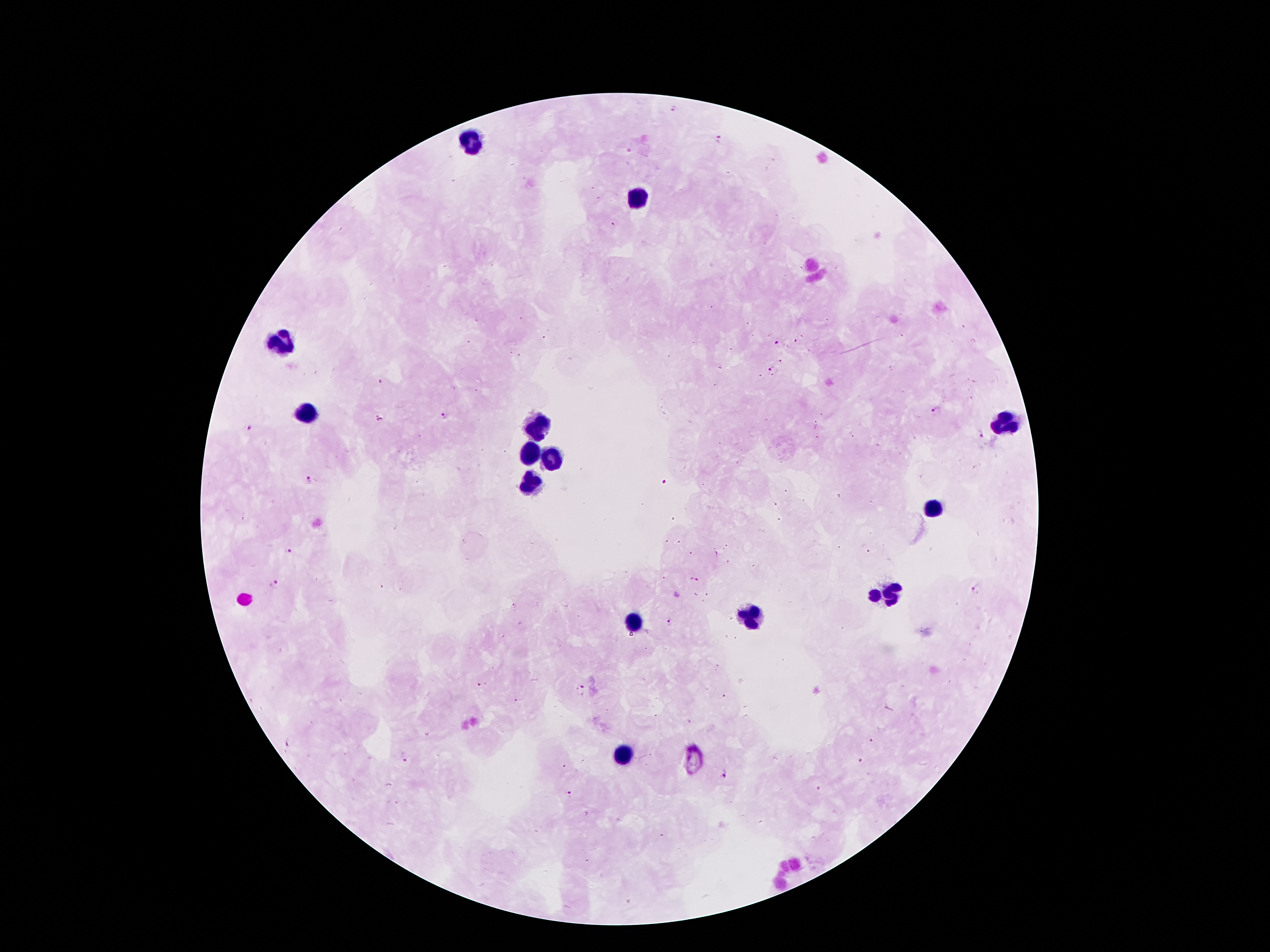

Approximate centers as [x, y] in pixels. Plasmodium parasite locations: [673, 109], [719, 139], [614, 224], [781, 342], [781, 359], [720, 367], [772, 370], [381, 382], [938, 411], [445, 416], [378, 417], [250, 427], [980, 435], [309, 481], [664, 482], [292, 551], [715, 554], [692, 578], [698, 580], [276, 584], [978, 587], [677, 595], [515, 607], [670, 622], [647, 632], [478, 684], [582, 686], [519, 700], [872, 740], [289, 742], [406, 758], [862, 761], [565, 767], [725, 776], [817, 789], [572, 793]. Leukocyte locations: [470, 136], [638, 201], [279, 346], [310, 413], [1007, 422], [537, 425], [531, 450], [554, 458], [528, 481], [932, 509], [876, 593], [893, 593], [750, 615], [635, 623], [624, 752]. 100x magnification. Thick blood film. One field from this slide. Giemsa stain. Image is 1270×952 pixels. Patient malaria status: positive for Plasmodium falciparum. Photographed through the microscope eyepiece with a smartphone camera.